Comment on the morphology of the erythrocytes.
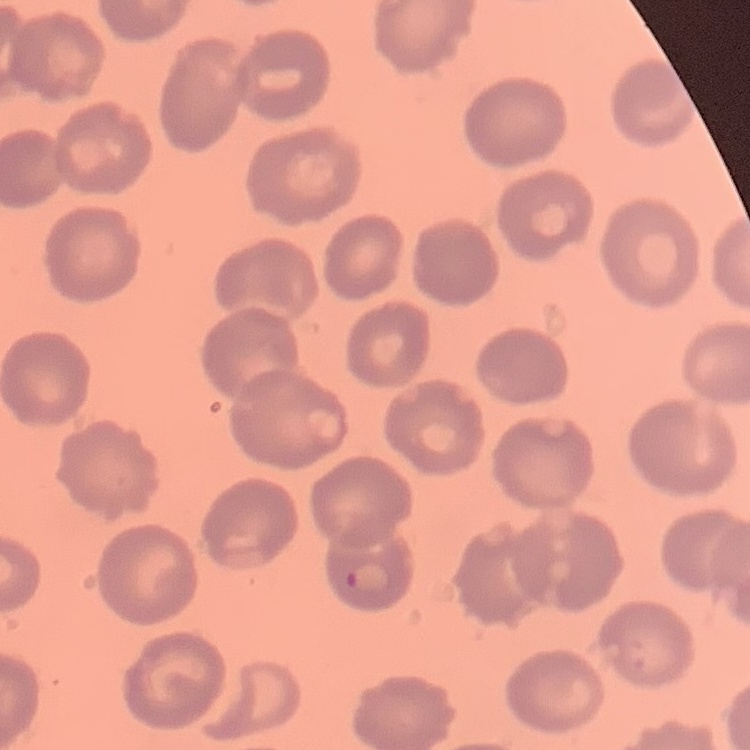
No rouleaux formation.

preparation = thin peripheral smear
stain = Field's or Giemsa
image type = square crop of a larger photomicrograph